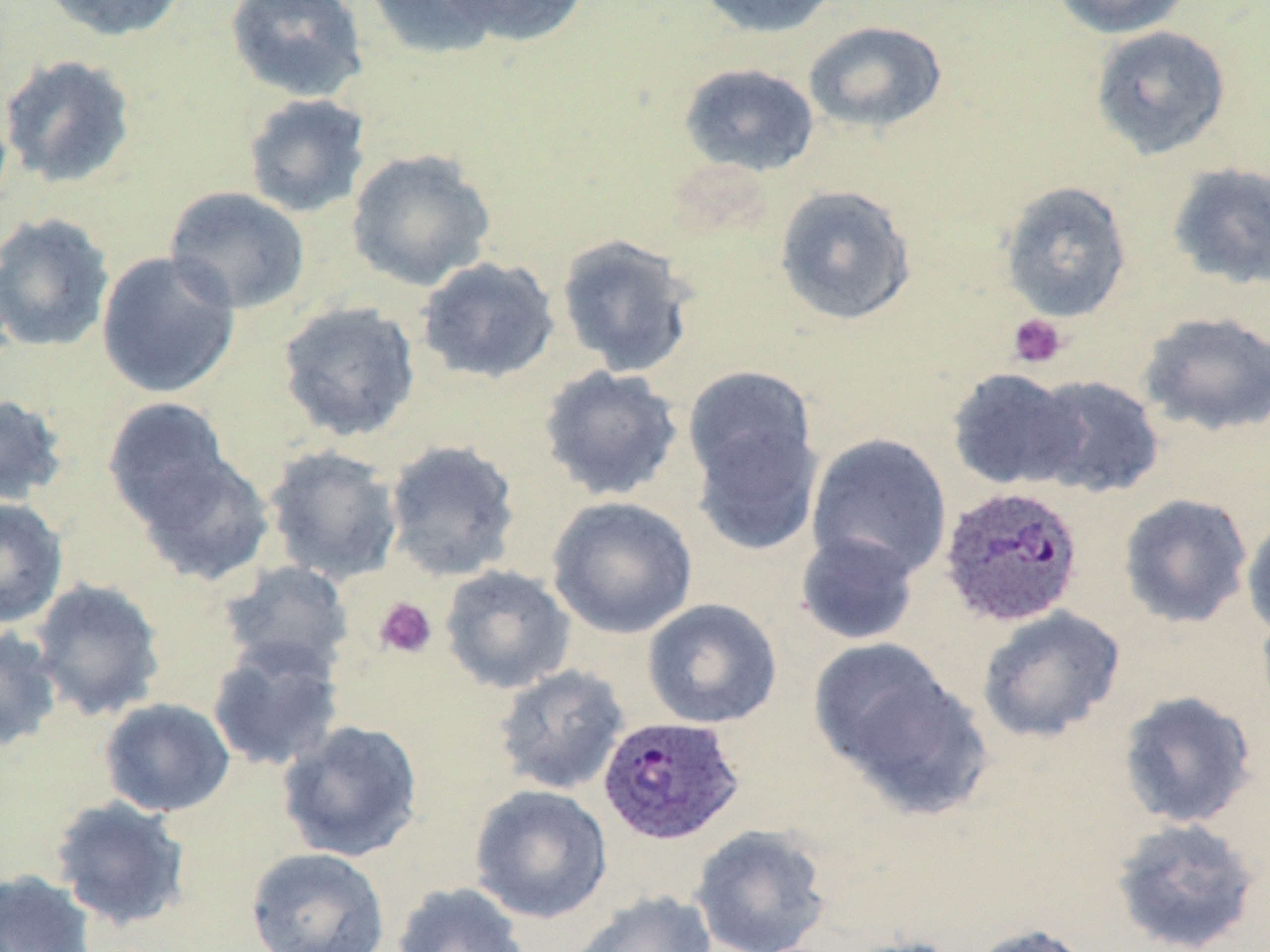
{
  "slide_level_diagnosis": "Plasmodium ovale",
  "modality": "optical microscopy",
  "stain": "May-Grünwald-Giemsa",
  "field_of_view": "one of a larger specimen",
  "magnification": "1000x",
  "plasmodium_ovale_infected_red_blood_cell_locations": "approximate bounding boxes as (x1, y1, x2, y2) in pixels: (938, 485, 1085, 628), (597, 715, 746, 847)",
  "image_size": "1270×952 pixels",
  "uninfected_red_blood_cell_locations": "approximate bounding boxes as (x1, y1, x2, y2) in pixels: (39, 0, 188, 42), (224, 0, 369, 103), (364, 0, 508, 61), (439, 0, 592, 47), (694, 0, 844, 38), (1051, 0, 1194, 39), (803, 20, 948, 134), (1089, 25, 1232, 160), (0, 53, 137, 189), (678, 62, 820, 177), (241, 93, 372, 219), (345, 149, 497, 291), (1167, 162, 1270, 290), (998, 180, 1133, 323), (773, 184, 917, 327), (164, 186, 311, 315), (0, 212, 115, 354), (555, 233, 699, 378), (96, 250, 241, 398), (416, 255, 560, 384), (276, 300, 422, 443), (1138, 311, 1270, 437), (538, 364, 684, 503), (681, 365, 822, 510), (946, 367, 1084, 491), (1027, 374, 1164, 499), (0, 393, 69, 507), (102, 397, 233, 525), (806, 432, 952, 583), (383, 440, 521, 582), (263, 445, 404, 585), (131, 448, 276, 587), (1118, 493, 1253, 629), (547, 495, 699, 640), (0, 496, 68, 629), (1241, 510, 1270, 641), (794, 531, 921, 646), (219, 560, 354, 677), (439, 564, 576, 695), (28, 578, 167, 722), (641, 598, 783, 729), (976, 606, 1126, 744), (0, 624, 63, 753), (808, 636, 972, 793), (206, 638, 345, 773), (493, 664, 630, 796), (1117, 690, 1258, 829), (99, 697, 235, 817), (276, 718, 425, 862), (469, 784, 613, 924), (49, 796, 193, 931), (1109, 816, 1262, 952), (690, 824, 831, 952), (245, 847, 390, 952), (0, 868, 96, 952), (391, 882, 529, 952), (569, 890, 717, 952), (967, 922, 1094, 952), (838, 935, 968, 952)",
  "preparation": "thin blood film",
  "platelet_locations": "approximate bounding boxes as (x1, y1, x2, y2) in pixels: (1008, 314, 1068, 369), (373, 597, 438, 659)"
}